Identify the parasite.
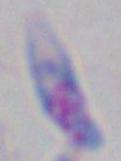

This is Toxoplasma gondii.

Photomicrograph. Captured at 1000x magnification.